Locate every blood parasite and identify its species.
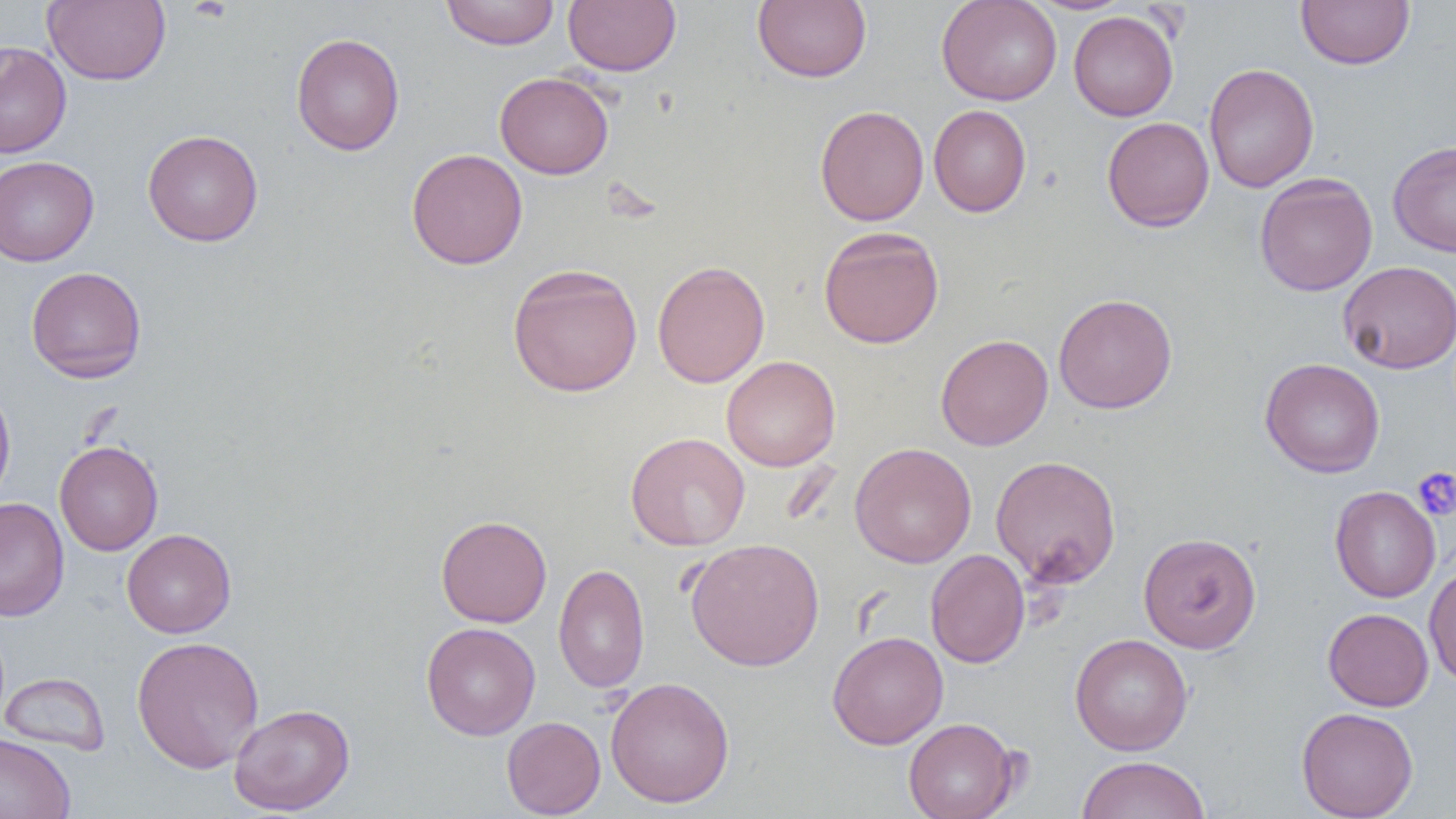

No blood parasites observed.

Approximate bounding boxes as [x1, y1, x2, y2] in pixels. Uninfected red blood cell locations: [43, 0, 171, 86], [440, 0, 560, 50], [563, 0, 681, 76], [936, 0, 1062, 105], [1027, 0, 1134, 15], [1296, 0, 1415, 70], [753, 1, 872, 83], [1069, 11, 1178, 121], [291, 32, 405, 155], [0, 42, 72, 158], [1204, 63, 1319, 193], [494, 72, 614, 179], [928, 104, 1032, 217], [814, 105, 929, 226], [1101, 116, 1214, 232], [142, 129, 263, 247], [1388, 140, 1456, 257], [406, 148, 528, 270], [0, 155, 99, 266], [1254, 172, 1378, 296], [818, 226, 945, 349], [652, 260, 770, 388], [1338, 260, 1456, 374], [507, 262, 643, 398], [25, 266, 147, 383], [1053, 293, 1177, 414], [935, 333, 1053, 450], [721, 355, 840, 471], [1259, 358, 1385, 478], [0, 382, 16, 508], [625, 432, 751, 551], [54, 440, 163, 555], [850, 442, 977, 568], [990, 454, 1122, 588], [1329, 485, 1441, 602], [0, 497, 69, 622], [436, 515, 552, 628], [121, 528, 236, 638], [1138, 532, 1262, 654], [685, 537, 825, 671], [926, 549, 1030, 668], [1424, 562, 1456, 688], [554, 563, 650, 694], [1323, 607, 1434, 711], [421, 622, 541, 741], [827, 631, 948, 750], [1070, 633, 1193, 756], [131, 635, 264, 773], [1, 672, 110, 756], [605, 677, 735, 807], [228, 703, 355, 815], [1296, 707, 1419, 819], [502, 716, 606, 818], [903, 717, 1020, 819], [0, 732, 76, 819], [1076, 755, 1211, 819]. Platelet locations: [1412, 466, 1456, 521]. Slide-level diagnosis: no evidence of blood parasites. Optical microscopy. 1000x magnification. Single field of view. Thin blood film. Image is 1456×819 pixels.